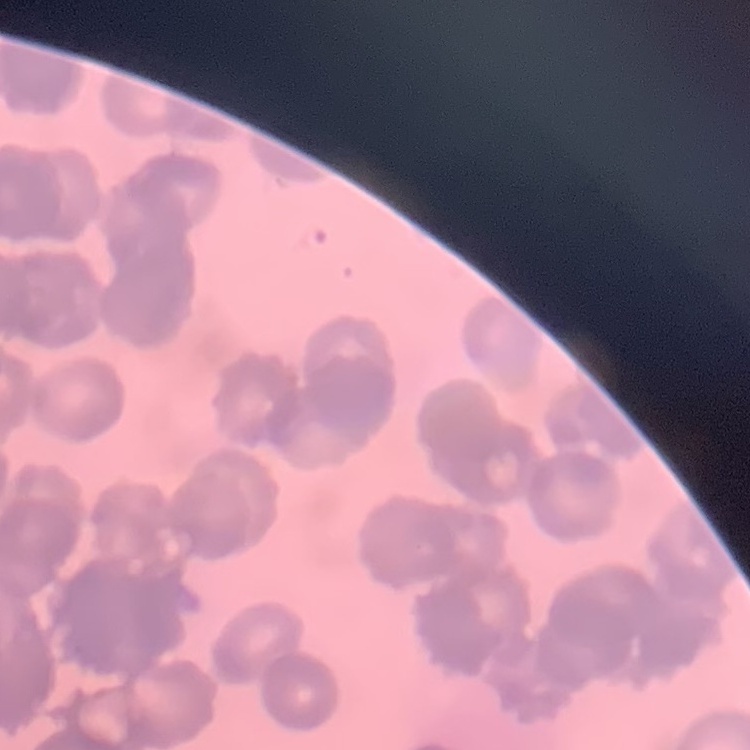

{
  "red_blood_cell_morphology": "rouleaux formation",
  "image_type": "square crop of a larger photomicrograph",
  "preparation": "thin blood smear",
  "stain": "Field's or Giemsa"
}